Name the parasite shown.
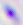

This is Toxoplasma gondii.

modality = micrograph
magnification = 400x